Assess this cell for malaria.
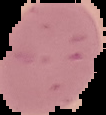
It is uninfected.

Summary:
  - Image size: 106×115 pixels
  - Preparation: thin blood smear
  - Image type: segmented cell region on a black background